Outline each Plasmodium falciparum parasite and classify it by life-cycle stage.
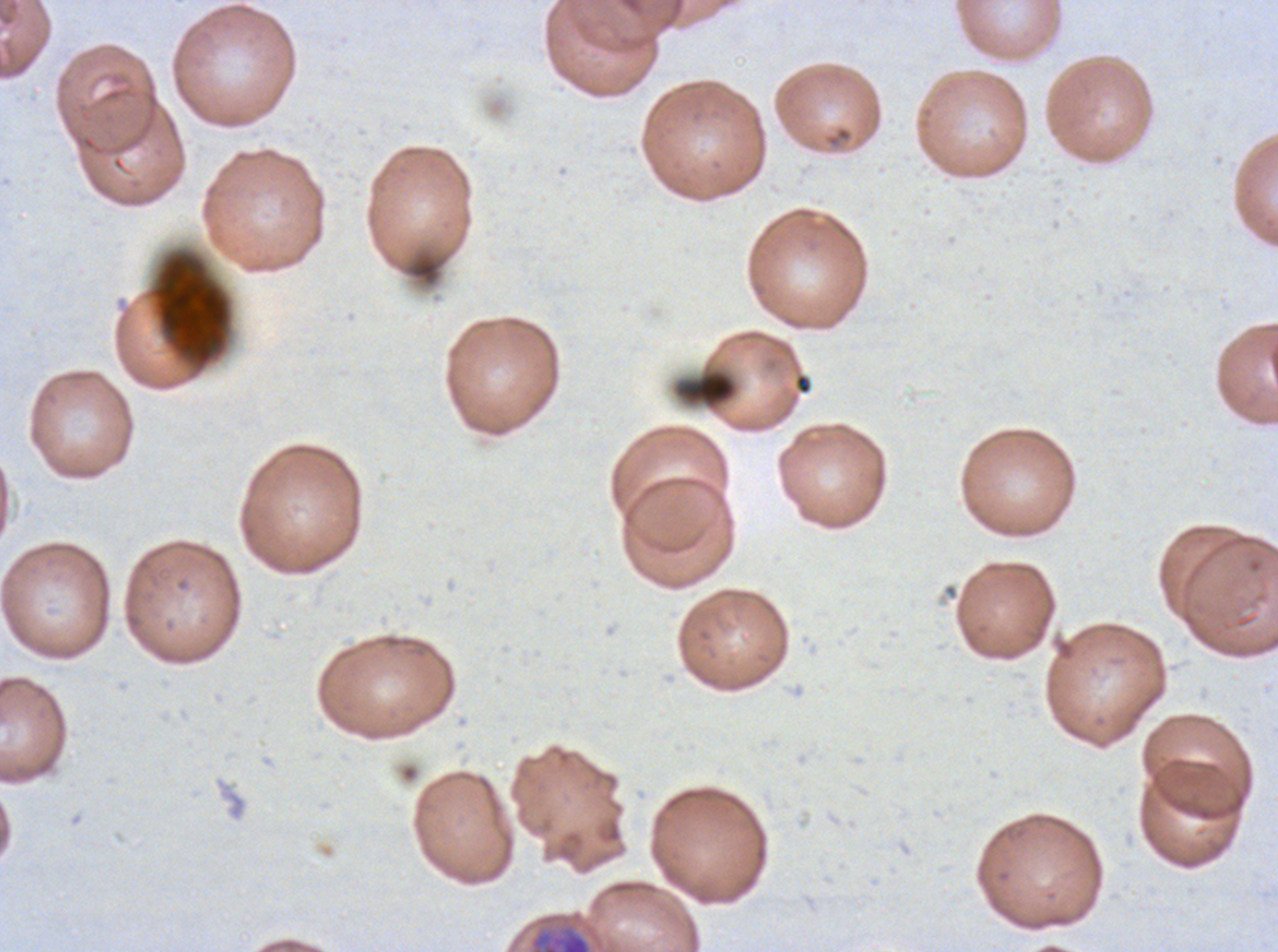
Approximate bounding boxes as (x1, y1, x2, y2) in pixels.
Early schizonts: (529, 924, 592, 951).
No rings, late-ring/early-trophozoite forms, mid trophozoites, late trophozoites, late schizonts, segmenters, or gametocytes observed.

Debris locations: (148, 250, 232, 371), (674, 368, 738, 410). Thin blood smear. Giemsa stain. Image is 1278×952 pixels. One sub-image of a larger composite. Ex-vivo Plasmodium falciparum culture from a patient in The Gambia, grown for 24 to 48 hours.